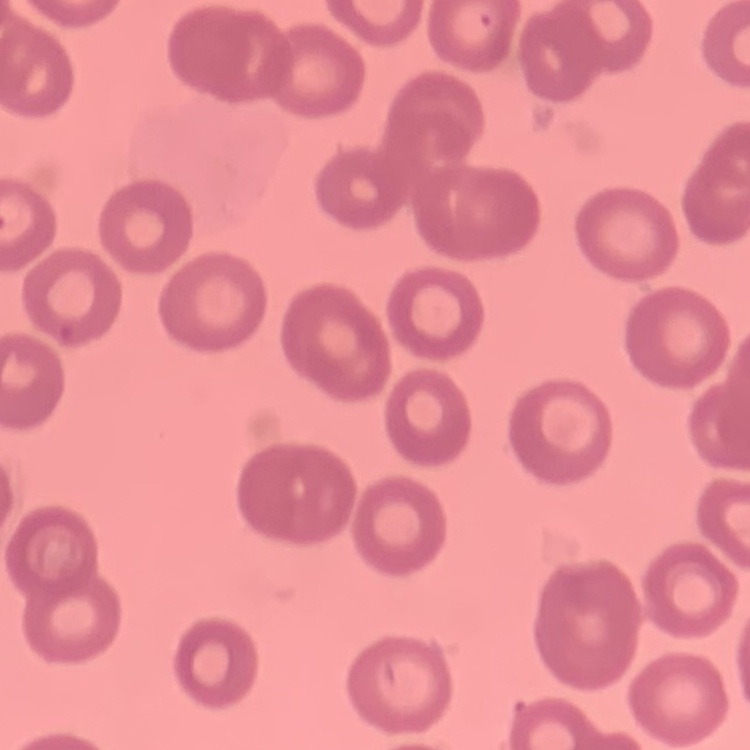

Summary:
  - Red blood cell morphology: no rouleaux formation
  - Preparation: thin peripheral smear
  - Image type: square crop of a larger photomicrograph
  - Stain: Field's or Giemsa